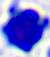

modality = photomicrograph
magnification = 400x
identification = leukocyte